Name the parasite shown.
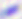

This is Toxoplasma gondii.

Summary:
  - Magnification: 400x
  - Modality: micrograph